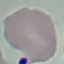
Result: no malaria parasites seen. Giemsa stain. Thin blood smear. Acquired by smartphone through the microscope eyepiece. Automatically extracted cell patch, resized to 64 × 64 pixels.